Identify the parasite.
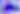
This is Toxoplasma gondii.

modality = micrograph
magnification = 400x